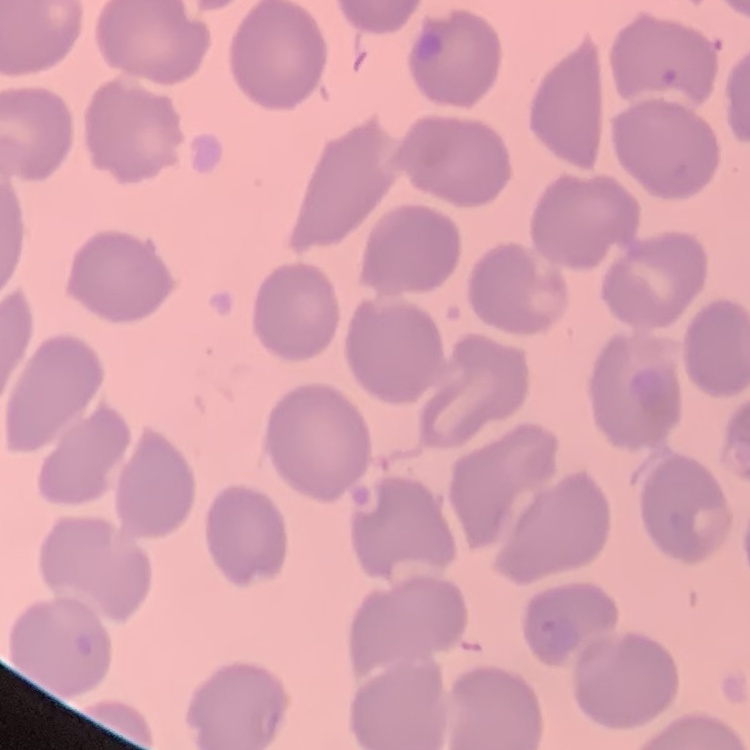
erythrocyte_morphology: no rouleaux formation
stain: Field's or Giemsa
image_type: square crop of a larger photomicrograph
preparation: thin peripheral smear